Classify this cell by malaria status.
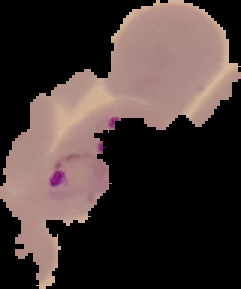

Parasitized.

Image is 241×289 pixels. Cell region segmented out of the field of view; the surrounding area is masked to black. From a thin blood smear.